Identify the cell.
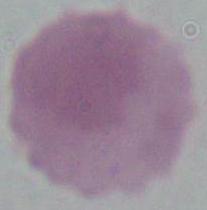

An erythrocyte.

magnification = 1000x
modality = photomicrograph